Point out each leukocyte.
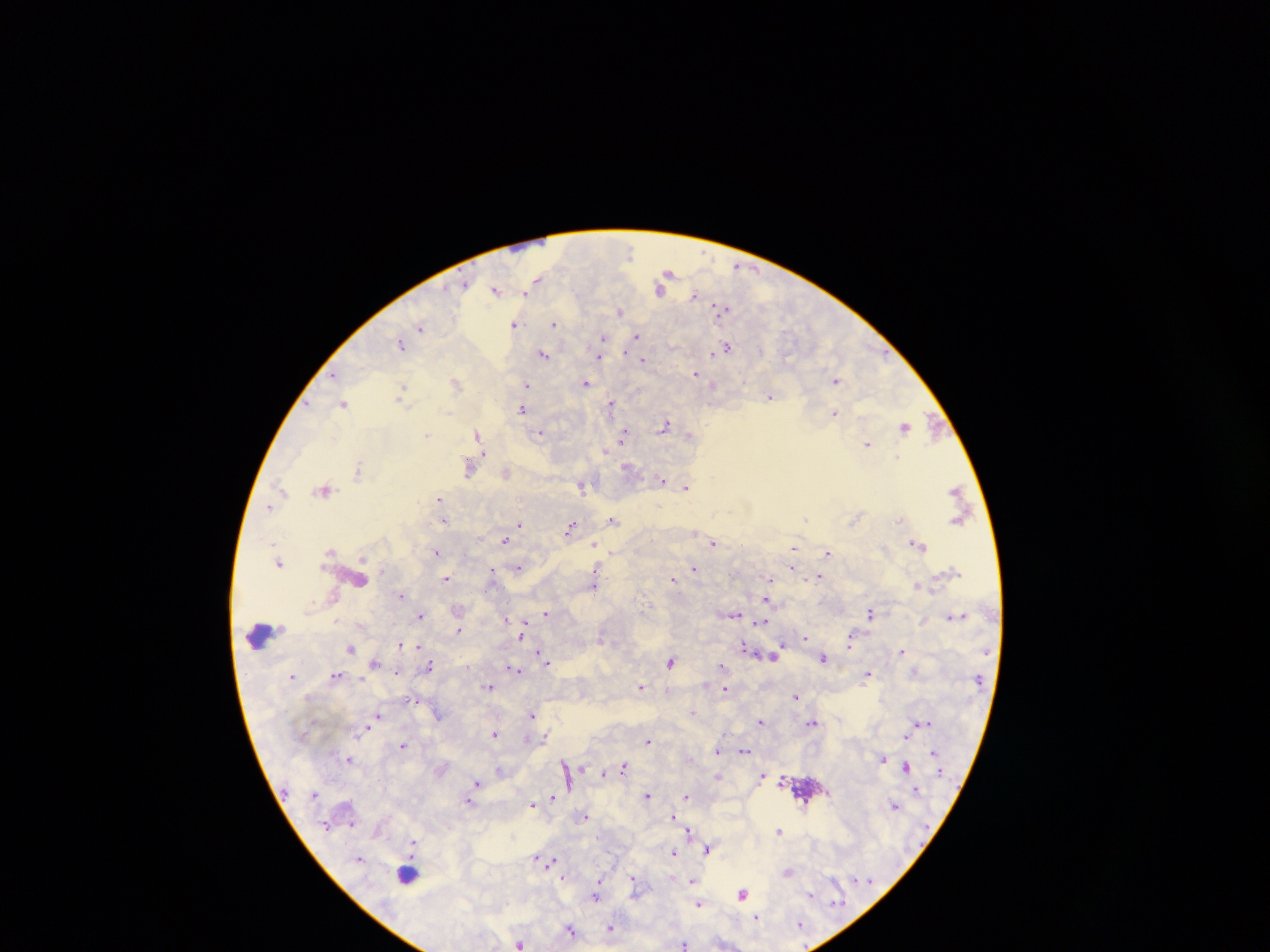
Approximate centers as {x, y} in pixels.
Leukocytes: {531, 245}, {263, 635}, {408, 872}.

country: Ghana
preparation: thick blood smear
field_of_view: single
image_size: 1270×952 pixels
capture: mobile-phone photograph through a microscope
plasmodium_parasite_locations: 'approximate centers as {x, y} in pixels: {629, 252}, {738, 266}, {669, 272}, {537, 279}, {465, 285}, {660, 289}, {495, 291}, {527, 293}, {695, 296}, {725, 309}, {620, 312}, {515, 324}, {554, 324}, {420, 327}, {637, 336}, {603, 338}, {401, 346}, {727, 346}, {760, 350}, {713, 353}, {544, 355}, {599, 356}, {643, 360}, {696, 373}, {333, 375}, {836, 380}, {586, 382}, {457, 383}, {526, 386}, {714, 386}, {401, 391}, {770, 397}, {343, 403}, {610, 406}, {522, 409}, {834, 413}, {665, 425}, {904, 426}, {933, 427}, {540, 433}, {427, 434}, {477, 434}, {625, 435}, {689, 436}, {867, 444}, {605, 450}, {897, 457}, {627, 467}, {469, 468}, {358, 469}, {506, 473}, {661, 479}, {581, 486}, {281, 487}, {686, 487}, {324, 489}, {439, 499}, {268, 506}, {613, 519}, {806, 519}, {899, 519}, {444, 521}, {520, 524}, {570, 528}, {504, 539}, {714, 542}, {917, 543}, {595, 545}, {793, 548}, {329, 550}, {437, 552}, {827, 552}, {279, 562}, {792, 568}, {518, 569}, {694, 569}, {596, 571}, {492, 574}, {446, 578}, {819, 578}, {673, 579}, {360, 581}, {769, 581}, {594, 585}, {917, 585}, {401, 595}, {768, 599}, {547, 612}, {871, 613}, {734, 615}, {952, 616}, {420, 617}, {507, 618}, {761, 623}, {524, 628}, {459, 630}, {522, 635}, {851, 638}, {805, 639}, {400, 645}, {418, 646}, {781, 646}, {351, 647}, {745, 647}, {901, 651}, {776, 654}, {542, 656}, {824, 658}, {546, 661}, {671, 661}, {375, 663}, {429, 665}, {721, 666}, {514, 668}, {396, 674}, {868, 674}, {336, 675}, {293, 676}, {641, 686}, {490, 687}, {724, 688}, {795, 696}, {693, 712}, {532, 714}, {438, 715}, {378, 717}, {761, 721}, {811, 722}, {922, 723}, {363, 730}, {494, 734}, {906, 734}, {546, 735}, {648, 740}, {403, 745}, {717, 751}, {745, 751}, {933, 752}, {349, 759}, {883, 759}, {565, 764}, {624, 767}, {905, 767}, {500, 769}, {605, 773}, {763, 775}, {718, 777}, {476, 782}, {916, 790}, {648, 795}, {553, 796}, {686, 797}, {470, 801}, {538, 801}, {533, 805}, {896, 805}, {586, 816}, {674, 816}, {352, 823}, {778, 831}, {689, 832}, {413, 843}, {708, 849}, {674, 853}, {537, 857}, {360, 859}, {547, 860}, {788, 872}, {563, 877}, {634, 879}, {693, 881}, {743, 893}, {596, 895}, {811, 895}, {699, 904}, {756, 918}, {800, 924}, {611, 927}, {570, 929}, {520, 944}, {684, 944}'